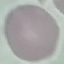

result = no malaria parasites seen
image type = automatically extracted cell patch, resized to 64 × 64 pixels
preparation = thin blood smear
capture = smartphone through the microscope eyepiece
stain = Giemsa